Evaluate for malaria.
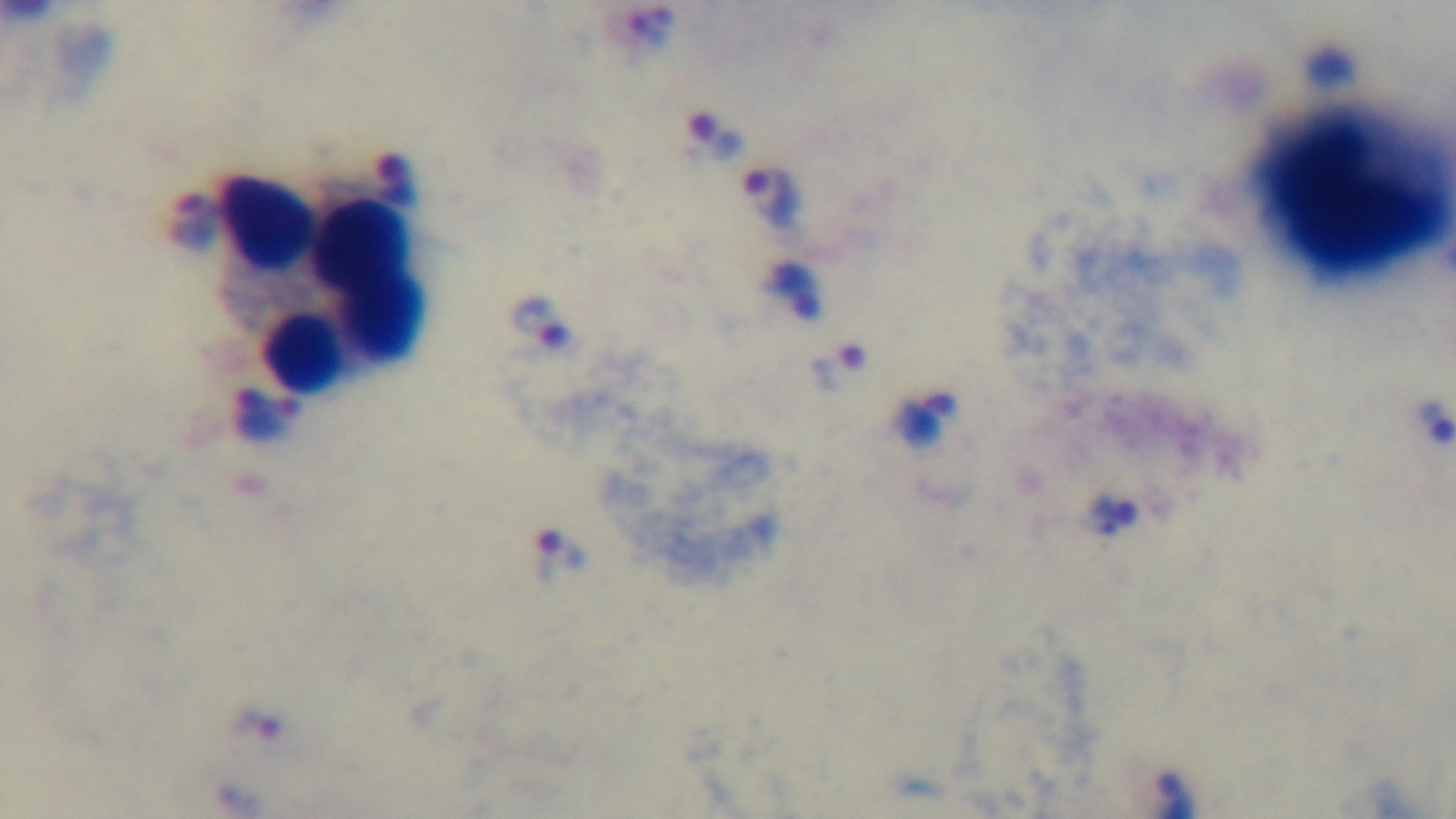
Infected.

preparation = thick
field of view = single
capture = mounted 4K digital camera
objective = 100x oil immersion
stain = Giemsa
modality = light microscopy